Assess this cell for malaria.
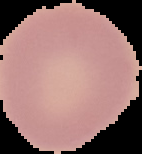
Uninfected.

Image is 142×154 pixels. Cell region segmented out of the field of view; the surrounding area is masked to black. From a thin blood smear.